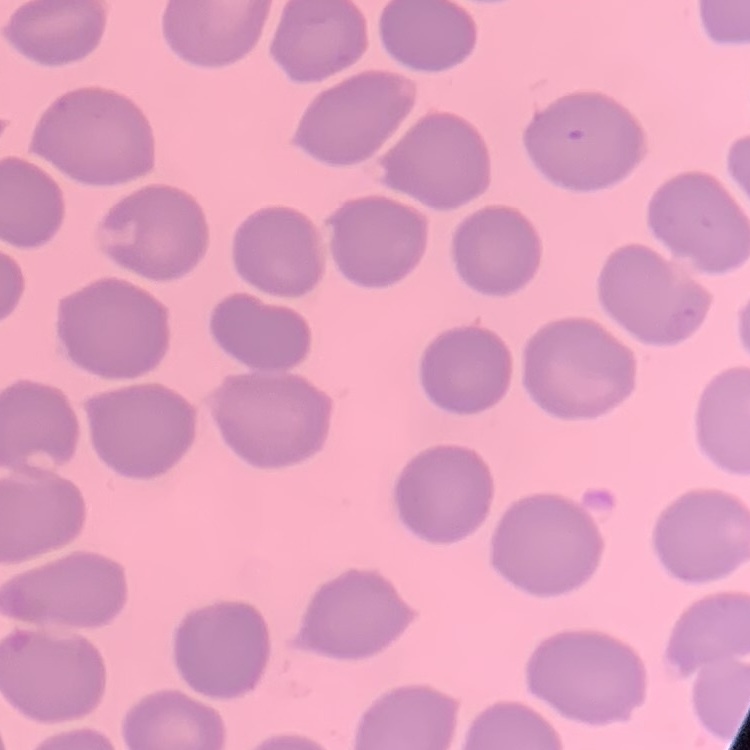 The erythrocytes exhibit no rouleaux formation. One tile cut from a larger photomicrograph. Thin peripheral smear. Field's or Giemsa stain.